Assess this cell for malaria.
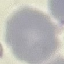
It is uninfected.

Photographed with a smartphone camera at the microscope eyepiece. Giemsa-stained preparation. Thin blood smear. Automatically extracted cell patch, resized to 64 × 64 pixels.